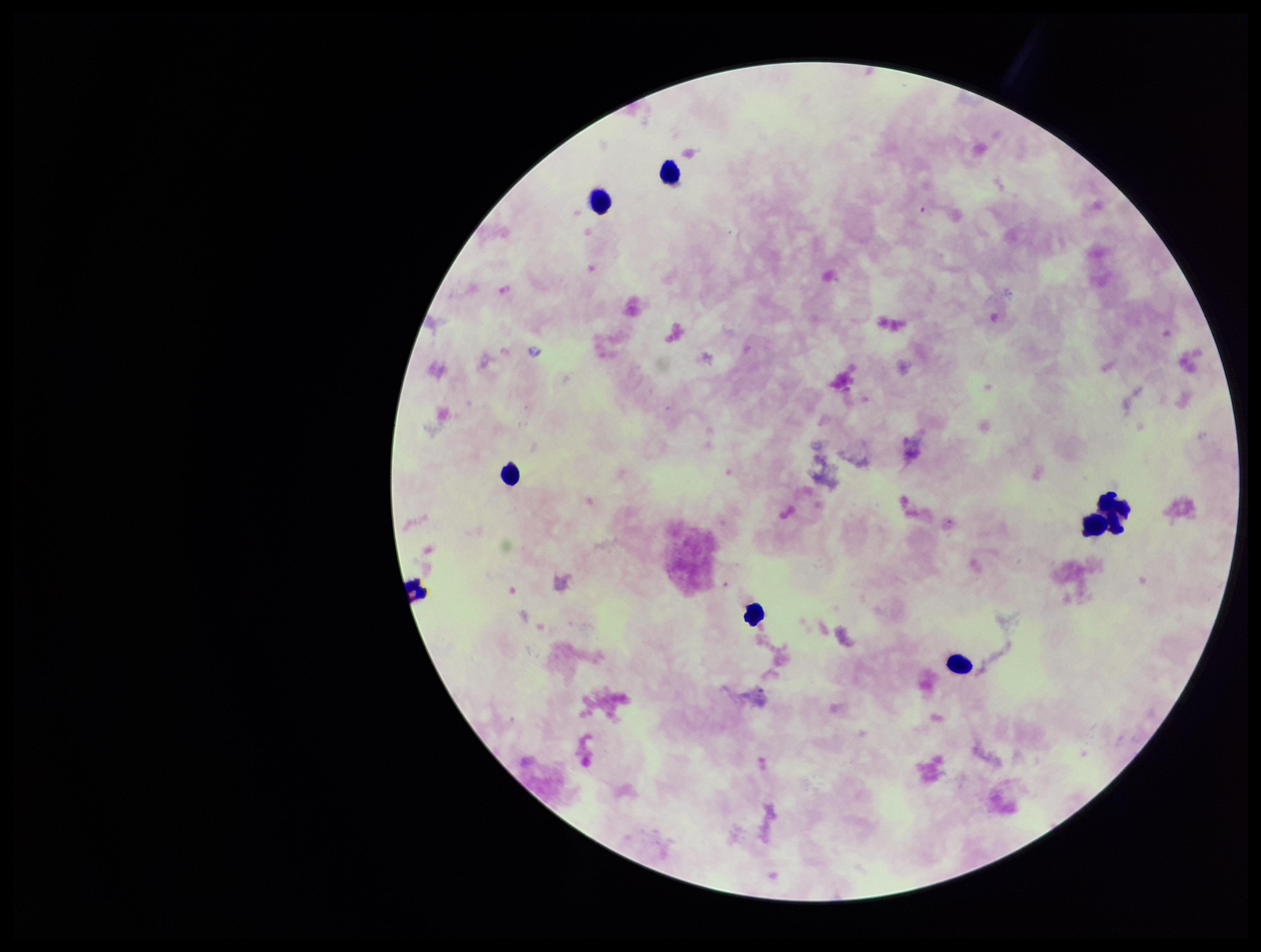 Parasite count: 0. Image is 1261×952 pixels. Plasmodium parasites: none seen. Patient malaria status: negative. Smartphone photograph taken through the eyepiece of a microscope. Giemsa stain. Single field of view. Leukocyte count: 8. Preparation: thick blood smear.